Report the malaria status of this cell.
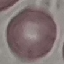

It is uninfected.

Summary:
  - Preparation: thin blood smear
  - Image type: automatically extracted cell patch, resized to 64 × 64 pixels
  - Stain: Giemsa
  - Capture: smartphone through the microscope eyepiece